State which parasite is depicted.
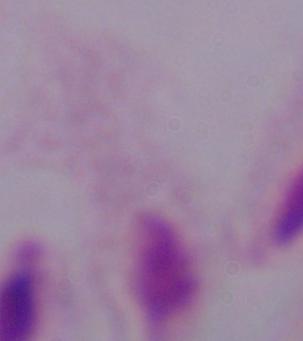
This is a trichomonad.

Captured at 1000x magnification. Micrograph.